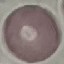
Summary:
  - Malaria status: uninfected
  - Image type: automatically extracted cell patch, resized to 64 × 64 pixels
  - Preparation: thin blood smear
  - Capture: smartphone through the microscope eyepiece
  - Stain: Giemsa